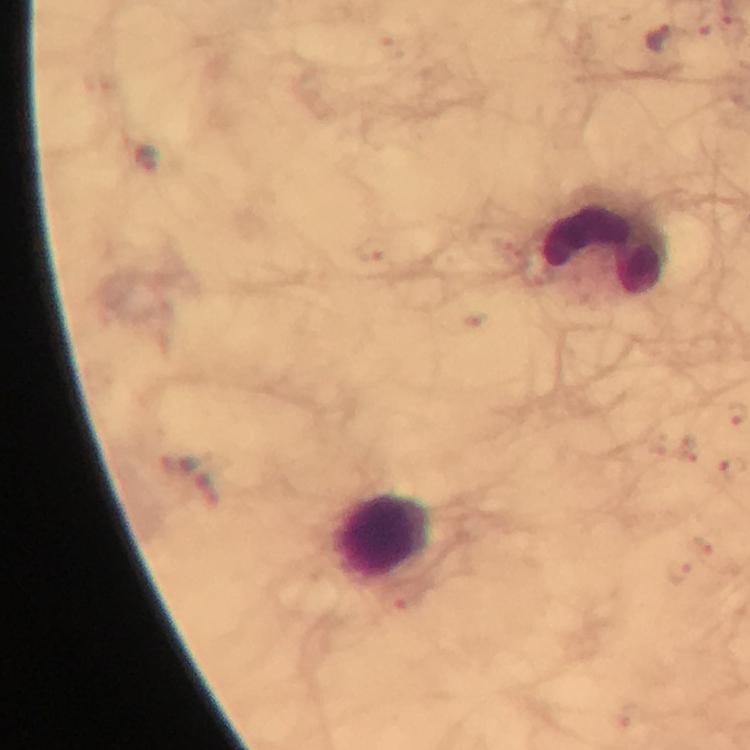 Approximate centers as (x, y) in pixels. Plasmodium parasite locations: (731, 28), (661, 36), (146, 158), (375, 250), (702, 545), (678, 572), (398, 602). Leukocyte locations: (604, 243), (385, 536). Thick blood smear. Image is 750×750 pixels. Giemsa-stained preparation. Smartphone photograph taken through a microscope. 100x magnification. A crop from one field of view. From a diagnostic examination for malaria. Immersion oil was used.